State which parasite is depicted.
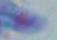

Toxoplasma gondii.

modality = micrograph
magnification = 1000x